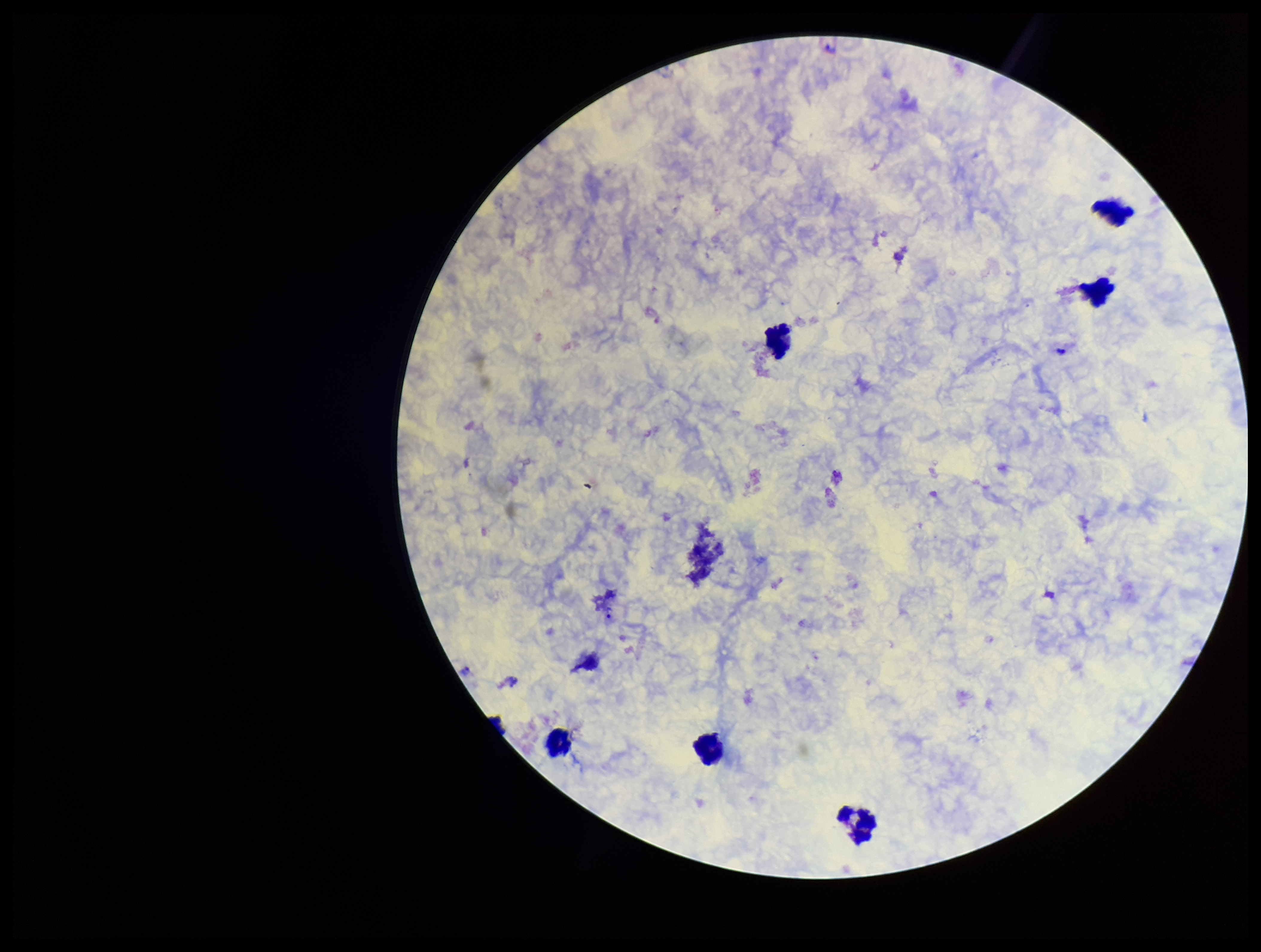

Summary:
  - Patient malaria status: positive
  - Leukocyte count: 6
  - Preparation: thick blood smear
  - Stain: Giemsa
  - Capture: smartphone photograph through the microscope eyepiece
  - Field of view: one from this slide
  - Image size: 1261×952 pixels
  - Plasmodium parasites: seen
  - Parasite count: 2
  - Species reported for this patient: Plasmodium vivax